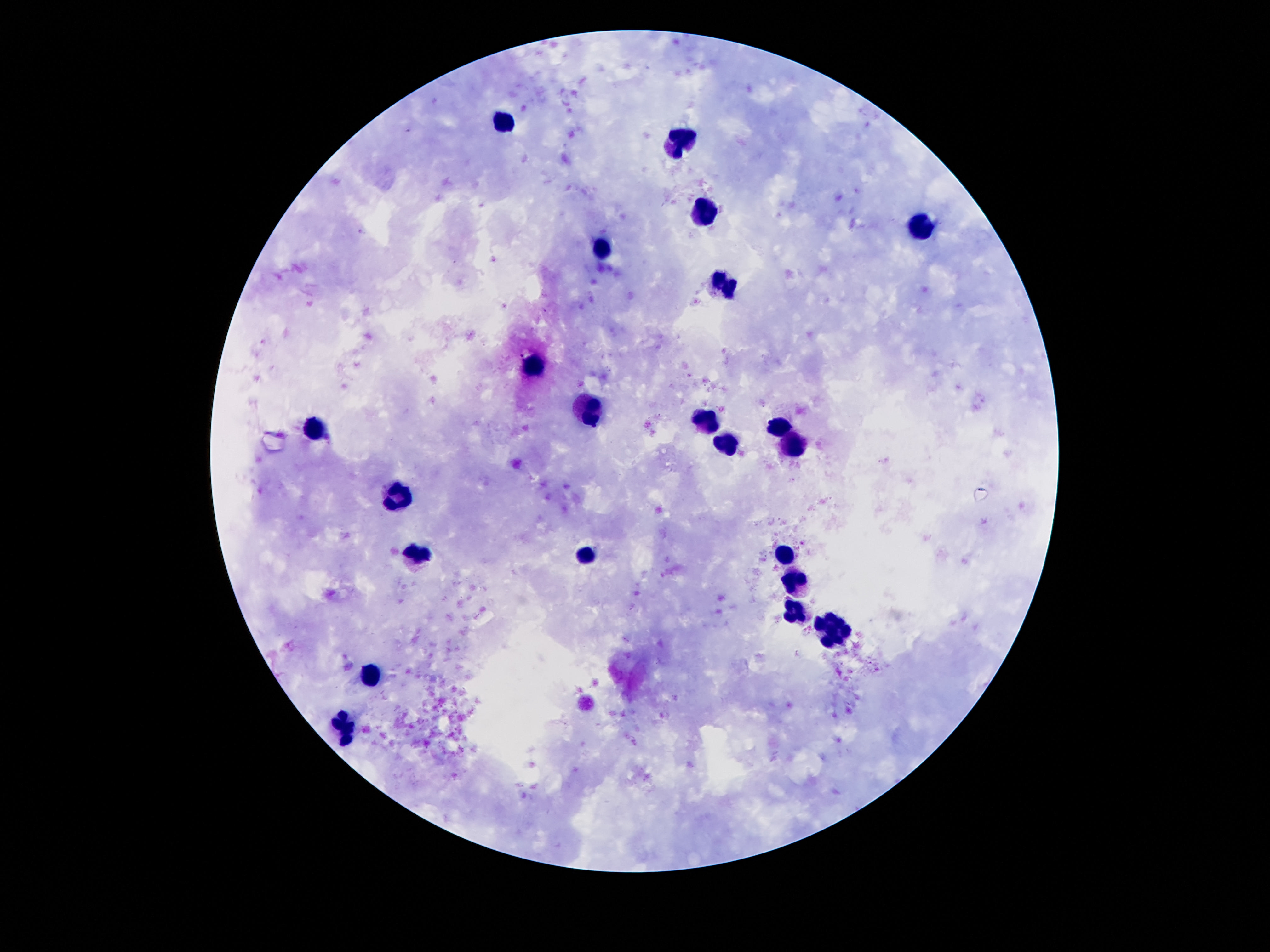

Approximate centers as (x, y) in pixels.
Summary:
  - Leukocyte locations: (504, 121), (679, 144), (704, 214), (922, 227), (601, 251), (724, 283), (533, 367), (588, 410), (706, 420), (776, 427), (314, 428), (791, 444), (726, 445), (396, 498), (588, 557), (785, 557), (417, 559), (796, 579), (793, 611), (371, 676), (347, 728)
  - Patient malaria status: not infected
  - Preparation: thick blood film
  - Capture: smartphone camera through the microscope eyepiece
  - Image size: 1270×952 pixels
  - Magnification: 100x
  - Field of view: single
  - Stain: Giemsa